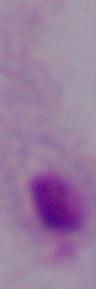

identification = trichomonad
modality = micrograph
magnification = 1000x